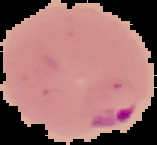

Summary:
  - Image type: segmented cell region on a black background
  - Malaria status: parasitized
  - Image size: 157×145 pixels
  - Preparation: thin blood smear